Outline each Plasmodium ovale-infected red blood cell.
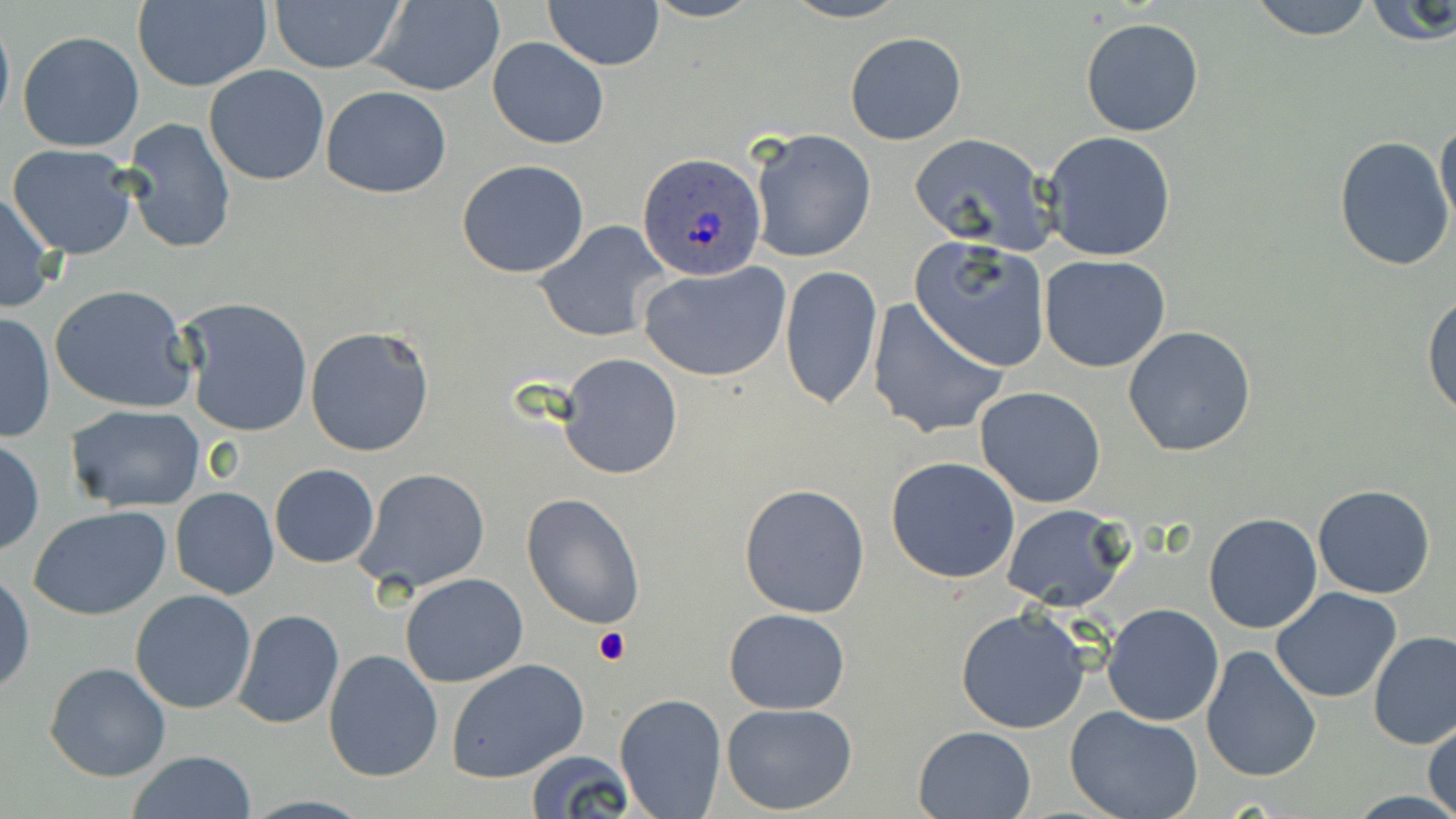

Approximate bounding boxes as named x1/y1/x2/y2 corners in pixels.
Plasmodium ovale-infected red blood cells: (x1=637, y1=152, x2=766, y2=281).

Summary:
  - Uninfected red blood cell locations: (x1=364, y1=0, x2=507, y2=97), (x1=543, y1=0, x2=664, y2=69), (x1=779, y1=0, x2=910, y2=24), (x1=1246, y1=0, x2=1378, y2=40), (x1=1361, y1=0, x2=1456, y2=48), (x1=132, y1=1, x2=271, y2=91), (x1=270, y1=1, x2=403, y2=75), (x1=0, y1=10, x2=14, y2=132), (x1=1080, y1=18, x2=1204, y2=136), (x1=844, y1=30, x2=967, y2=145), (x1=18, y1=31, x2=145, y2=153), (x1=487, y1=38, x2=609, y2=149), (x1=203, y1=65, x2=330, y2=185), (x1=320, y1=86, x2=451, y2=198), (x1=1435, y1=116, x2=1456, y2=234), (x1=121, y1=117, x2=235, y2=255), (x1=747, y1=128, x2=877, y2=263), (x1=1041, y1=130, x2=1177, y2=261), (x1=908, y1=133, x2=1055, y2=251), (x1=1335, y1=135, x2=1453, y2=270), (x1=8, y1=144, x2=138, y2=259), (x1=456, y1=160, x2=588, y2=278), (x1=0, y1=191, x2=59, y2=314), (x1=533, y1=220, x2=669, y2=343), (x1=909, y1=237, x2=1051, y2=373), (x1=1038, y1=254, x2=1171, y2=373), (x1=641, y1=262, x2=790, y2=382), (x1=780, y1=264, x2=882, y2=410), (x1=49, y1=284, x2=197, y2=414), (x1=1422, y1=290, x2=1456, y2=420), (x1=178, y1=298, x2=312, y2=438), (x1=868, y1=298, x2=1009, y2=441), (x1=1, y1=312, x2=56, y2=444), (x1=304, y1=324, x2=436, y2=458), (x1=1123, y1=326, x2=1257, y2=459), (x1=559, y1=354, x2=682, y2=479), (x1=975, y1=386, x2=1107, y2=507), (x1=65, y1=404, x2=206, y2=512), (x1=0, y1=438, x2=43, y2=556), (x1=886, y1=456, x2=1021, y2=583), (x1=269, y1=464, x2=379, y2=567), (x1=356, y1=468, x2=489, y2=596), (x1=737, y1=482, x2=870, y2=618), (x1=1313, y1=484, x2=1437, y2=599), (x1=171, y1=487, x2=278, y2=599), (x1=521, y1=491, x2=645, y2=629), (x1=1001, y1=503, x2=1132, y2=611), (x1=29, y1=506, x2=172, y2=620), (x1=1202, y1=512, x2=1322, y2=634), (x1=0, y1=572, x2=34, y2=695), (x1=400, y1=573, x2=529, y2=687), (x1=1270, y1=587, x2=1403, y2=703), (x1=130, y1=590, x2=257, y2=713), (x1=1103, y1=602, x2=1225, y2=725), (x1=954, y1=607, x2=1093, y2=735), (x1=231, y1=608, x2=344, y2=729), (x1=723, y1=608, x2=849, y2=713), (x1=1368, y1=630, x2=1456, y2=748), (x1=1200, y1=645, x2=1322, y2=783), (x1=323, y1=649, x2=443, y2=782), (x1=446, y1=658, x2=588, y2=782), (x1=44, y1=661, x2=172, y2=782), (x1=614, y1=692, x2=727, y2=818), (x1=720, y1=703, x2=859, y2=815), (x1=1064, y1=704, x2=1203, y2=819), (x1=1425, y1=716, x2=1456, y2=817), (x1=912, y1=725, x2=1037, y2=818), (x1=524, y1=749, x2=638, y2=818), (x1=127, y1=750, x2=256, y2=819)
  - Platelet locations: (x1=595, y1=627, x2=630, y2=666)
  - Slide-level diagnosis: Plasmodium ovale
  - Magnification: 1000x
  - Stain: May-Grünwald-Giemsa
  - Modality: light microscopy
  - Image size: 1456×819 pixels
  - Preparation: thin blood film
  - Field of view: single